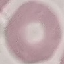
{
  "result": "negative for malaria parasites",
  "stain": "Giemsa",
  "image_type": "cell patch, automatically extracted from a larger field of view and resized to 64 × 64 pixels",
  "preparation": "thin blood film",
  "capture": "smartphone camera at the microscope eyepiece"
}